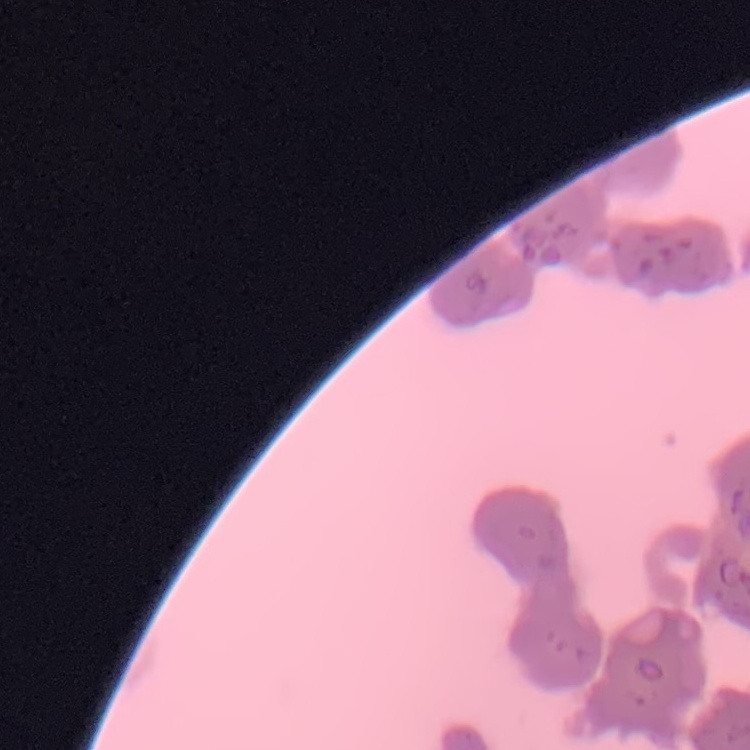

Summary:
  - Erythrocyte morphology: rouleaux formation
  - Stain: Field's or Giemsa
  - Image type: one tile cut from a larger photomicrograph
  - Preparation: thin blood smear